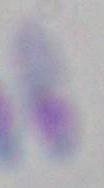

Summary:
  - Magnification: 1000x
  - Modality: photomicrograph
  - Identification: Toxoplasma gondii